Outline each blood parasite and name the species.
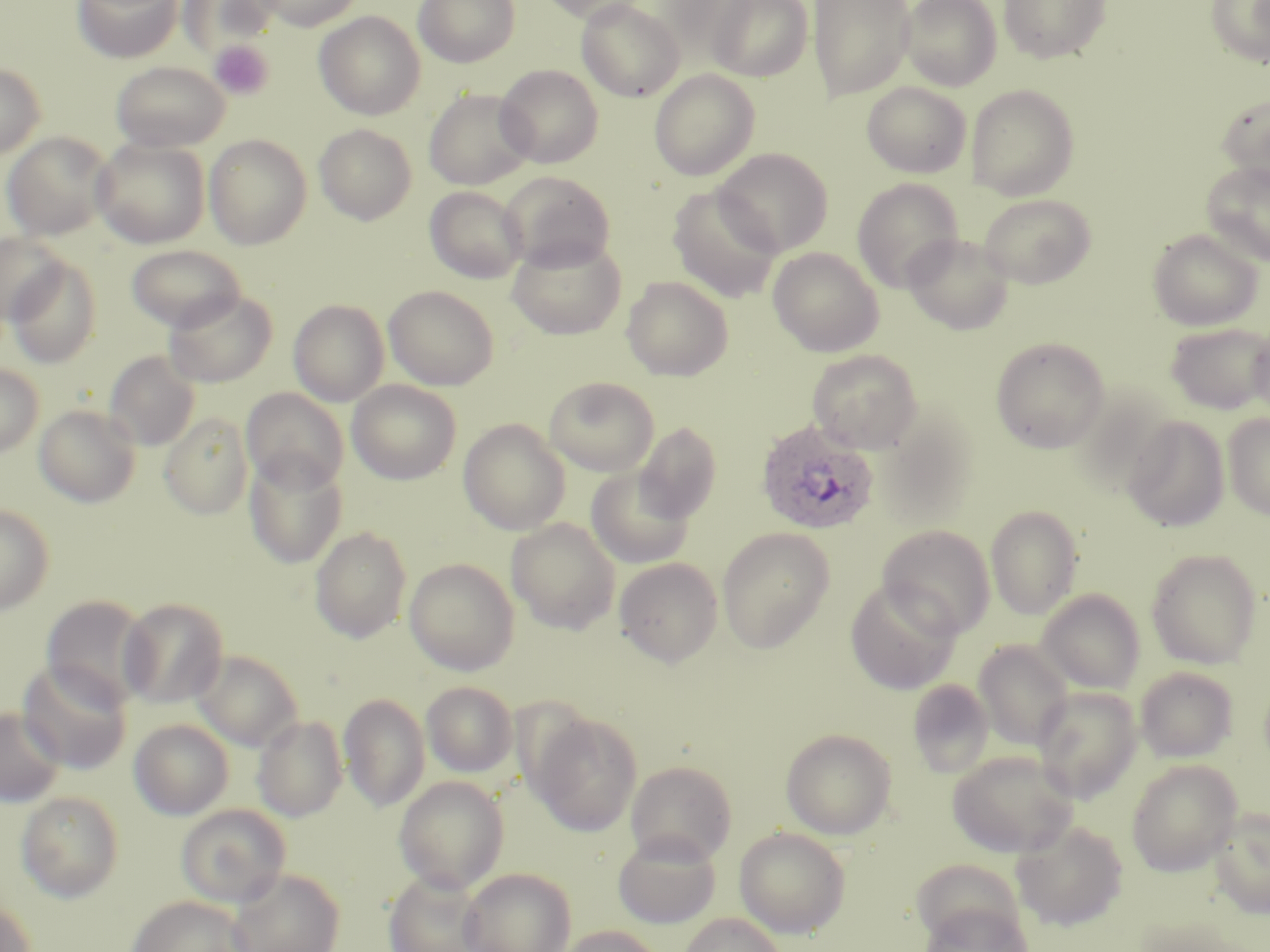
Approximate bounding boxes as (x1,y1)-(x2,y2) corner pairs in pixels.
Plasmodium ovale-infected red blood cells: (755,420)-(879,535).
No Plasmodium falciparum, Plasmodium malariae, Plasmodium vivax, Babesia divergens, or Trypanosoma brucei observed.

Uninfected red blood cell locations: (73,0)-(182,63), (178,0)-(281,57), (252,0)-(364,30), (413,0)-(521,67), (536,0)-(652,25), (708,0)-(814,82), (809,0)-(915,101), (901,0)-(1002,90), (999,0)-(1111,64), (1206,0)-(1270,67), (576,1)-(685,102), (314,11)-(426,120), (206,43)-(274,102), (110,61)-(230,152), (0,63)-(45,159), (496,64)-(604,168), (649,69)-(760,181), (862,81)-(971,178), (966,84)-(1080,200), (423,87)-(535,191), (1216,93)-(1270,187), (314,124)-(417,225), (2,132)-(113,241), (204,134)-(312,249), (91,138)-(210,248), (714,148)-(832,255), (1201,161)-(1270,268), (500,170)-(616,271), (852,178)-(964,291), (668,185)-(782,303), (424,186)-(527,283), (979,193)-(1096,289), (1148,229)-(1263,331), (0,233)-(68,326), (903,233)-(1014,335), (507,235)-(627,339), (126,244)-(246,332), (768,247)-(884,356), (5,256)-(103,369), (622,276)-(733,381), (384,285)-(499,390), (164,289)-(277,388), (289,299)-(389,406), (1165,322)-(1270,414), (1249,326)-(1270,423), (990,337)-(1110,453), (807,349)-(923,452), (104,350)-(200,451), (0,364)-(43,457), (544,376)-(660,476), (347,380)-(462,485), (241,388)-(349,492), (34,404)-(141,507), (162,412)-(253,519), (1222,413)-(1270,520), (877,414)-(980,529), (1121,415)-(1229,532), (458,418)-(570,535), (634,422)-(722,524), (243,453)-(347,568), (586,466)-(695,568), (0,504)-(54,615), (985,504)-(1083,620), (506,518)-(621,634), (309,525)-(412,643), (877,525)-(996,639), (717,527)-(835,654), (1146,548)-(1262,669), (614,557)-(723,667), (404,558)-(520,675), (845,580)-(961,695), (1036,589)-(1145,694), (40,595)-(153,708), (118,597)-(228,708), (973,641)-(1074,751), (192,649)-(304,752), (17,660)-(133,775), (1135,666)-(1238,763), (907,680)-(993,778), (422,681)-(518,778), (1032,686)-(1143,803), (339,693)-(430,812), (1,707)-(65,807), (528,710)-(643,836), (252,714)-(348,822), (129,719)-(234,819), (780,727)-(897,839), (947,749)-(1079,857), (1126,759)-(1242,876), (625,760)-(737,865), (394,776)-(509,894), (16,791)-(124,902), (175,804)-(291,907), (1208,807)-(1269,918), (1011,819)-(1129,932), (734,826)-(851,938), (612,831)-(721,929), (460,867)-(577,952), (225,868)-(346,952), (383,872)-(488,952), (128,895)-(252,951), (0,900)-(37,952), (918,902)-(1034,952), (679,913)-(788,952), (556,925)-(664,952). Platelet locations: (209,41)-(273,99). Slide-level diagnosis: Plasmodium ovale. Thin blood smear. Captured at 1000x magnification. Image is 1270×952 pixels. One field of a larger specimen. May-Grünwald-Giemsa stain. Optical microscopy.